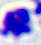

{
  "magnification": "400x",
  "identification": "white blood cell",
  "modality": "photomicrograph"
}